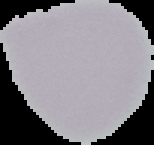

{
  "preparation": "thin blood film",
  "result": "negative for malaria parasites",
  "image_type": "segmented cell region on a black background",
  "image_size": "154×145 pixels"
}